Locate every Plasmodium parasite and every leukocyte.
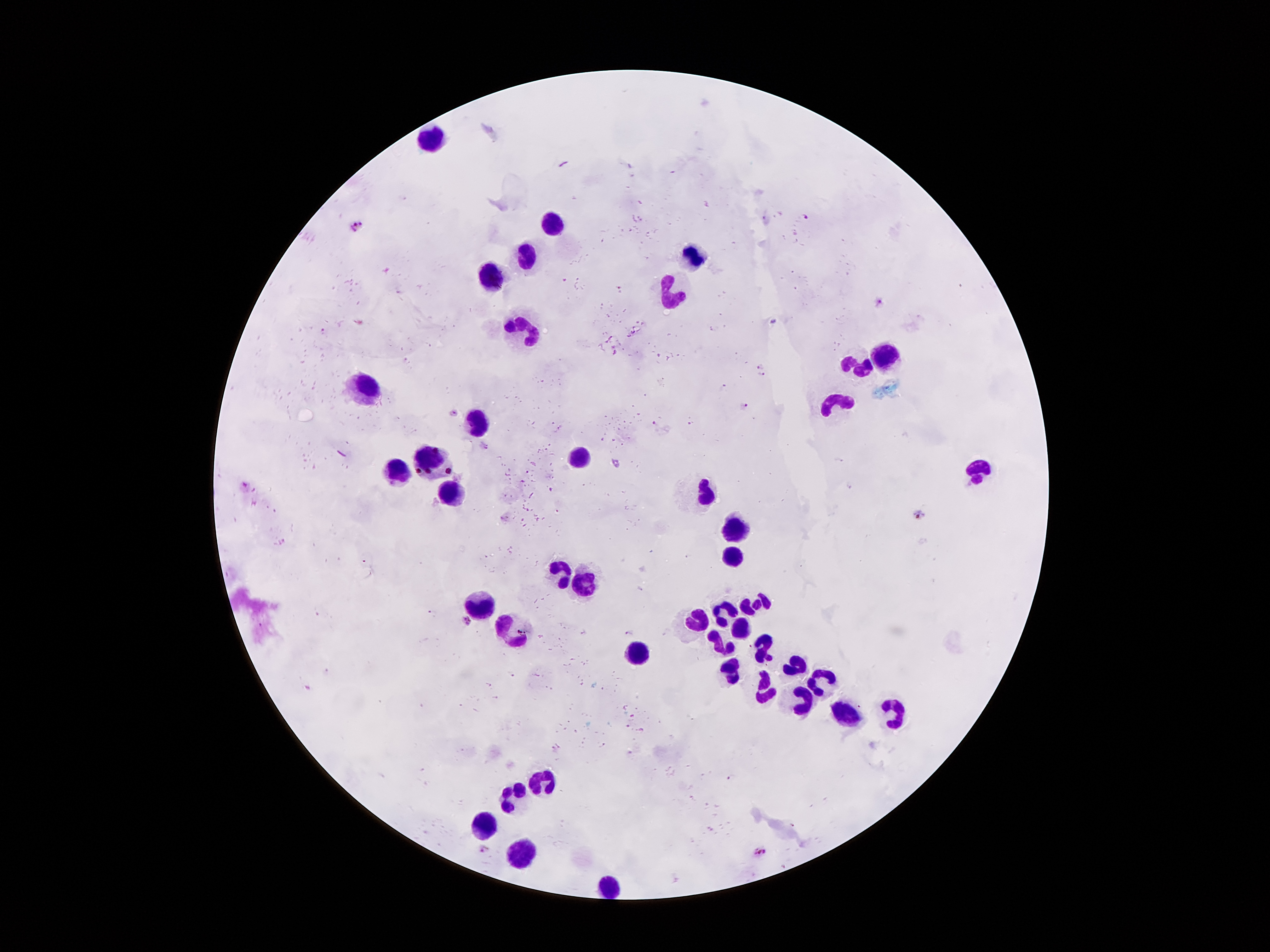

Approximate centers as (x, y) in pixels.
Plasmodium parasites: (807, 217), (358, 226), (880, 301), (759, 366), (763, 376), (743, 407), (454, 412), (919, 514), (467, 619), (484, 851), (759, 852).
Leukocytes: (431, 136), (555, 224), (527, 252), (695, 252), (493, 276), (671, 294), (525, 326), (887, 354), (857, 364), (365, 384), (837, 400), (477, 418), (579, 458), (431, 460), (397, 468), (977, 472), (705, 490), (449, 492), (739, 528), (733, 552), (561, 568), (587, 580), (481, 602), (755, 604), (725, 610), (693, 620), (739, 624), (513, 630), (723, 642), (765, 650), (641, 654), (797, 664), (731, 678), (819, 680), (763, 688), (799, 700), (845, 712), (897, 712), (551, 778), (515, 794), (487, 824), (519, 848), (609, 880).

Summary:
  - Magnification: 100x
  - Field of view: single
  - Patient malaria status: infected with Plasmodium falciparum
  - Preparation: thick blood smear
  - Capture: smartphone through the microscope eyepiece
  - Stain: Giemsa
  - Image size: 1270×952 pixels